Evaluate for malaria.
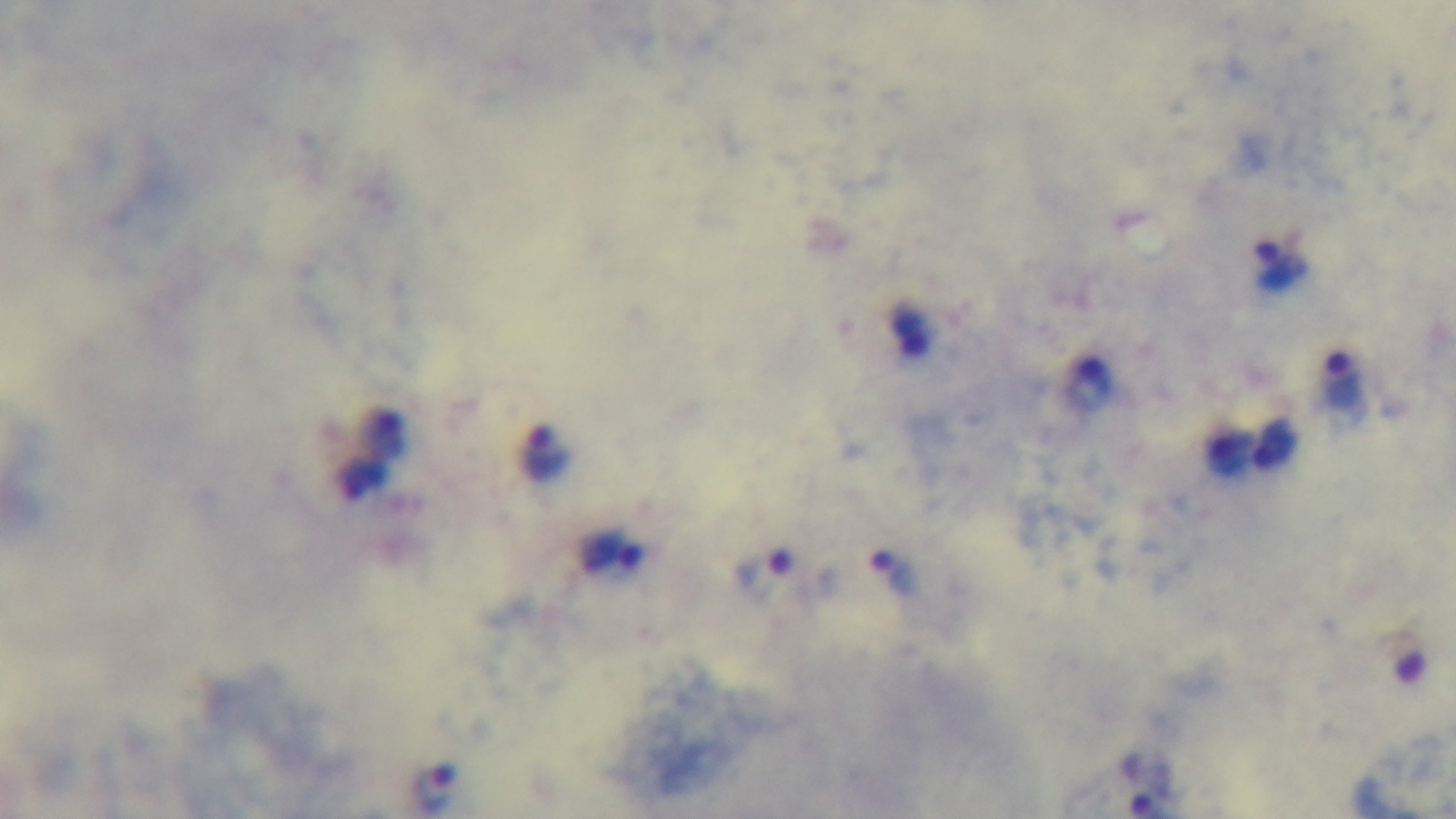

It is infected.

Summary:
  - Objective: 100x oil immersion
  - Field of view: one from the slide
  - Stain: Giemsa
  - Preparation: thick smear
  - Modality: light microscopy
  - Capture: mounted 4K digital camera